Outline each Plasmodium parasite.
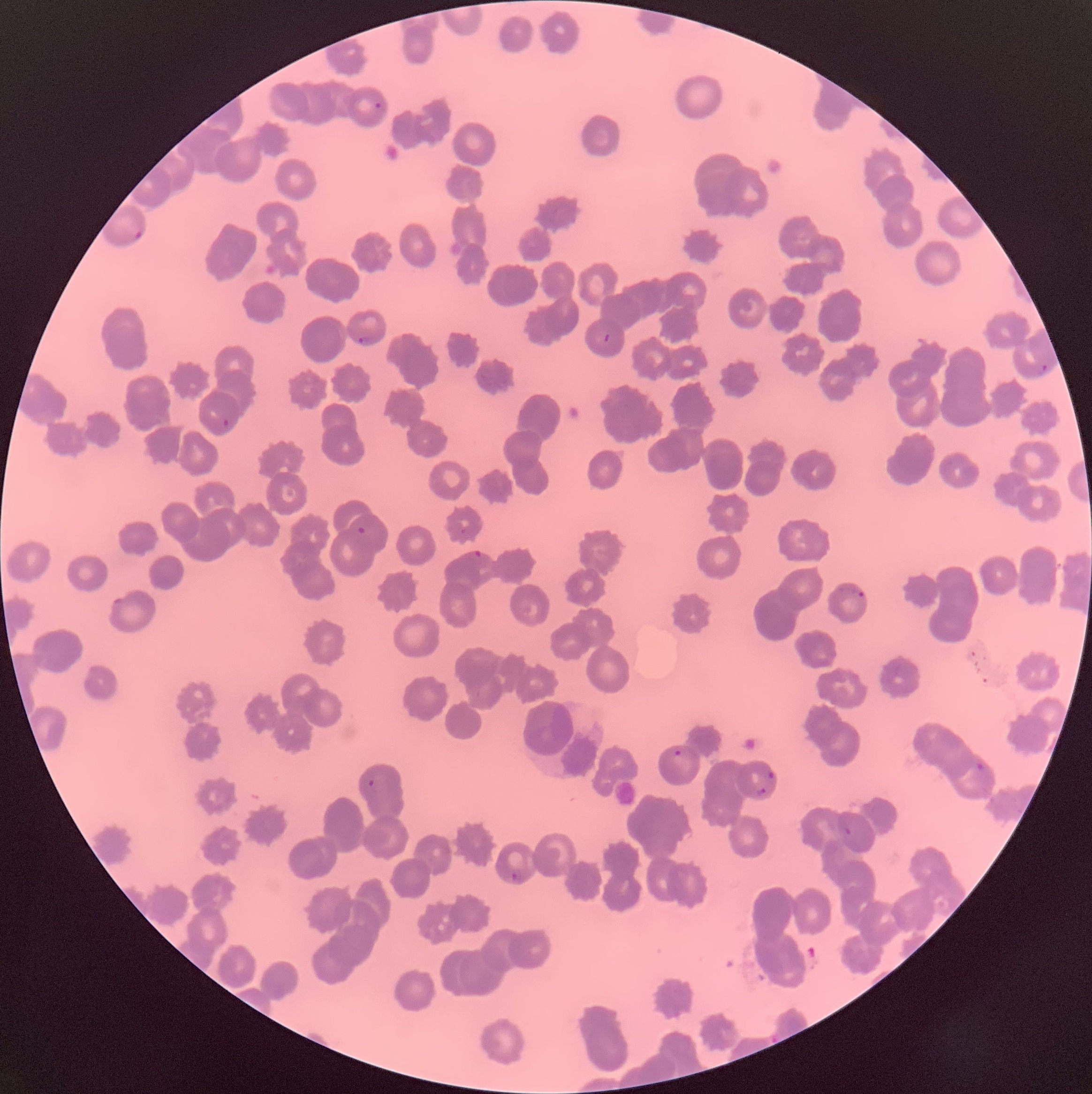
Approximate bounding boxes as [x1, y1, x2, y2] in pixels.
Plasmodium parasites: [373, 100, 384, 111], [126, 223, 143, 241], [603, 331, 612, 343], [355, 335, 376, 346], [1038, 362, 1050, 375], [221, 418, 231, 429], [356, 525, 368, 536], [460, 528, 468, 536], [473, 550, 483, 558], [855, 590, 866, 600], [112, 598, 128, 607], [672, 747, 688, 766], [973, 760, 987, 774], [765, 770, 776, 782], [366, 779, 379, 789], [752, 785, 768, 798], [842, 824, 855, 837], [510, 870, 524, 883].

Image is 1092×1094 pixels. Thin blood film. The red blood cells show rouleaux formation. Light microscopy.